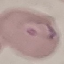
Result: malaria parasites identified. Thin blood film. Giemsa stain. Photographed with a smartphone camera at the microscope eyepiece. Automatically extracted cell patch, resized to 64 × 64 pixels.